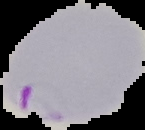
Image is 145×130 pixels. Cell region segmented out of the field of view; the surrounding area is masked to black. Malaria status: parasitized. From a thin blood smear.